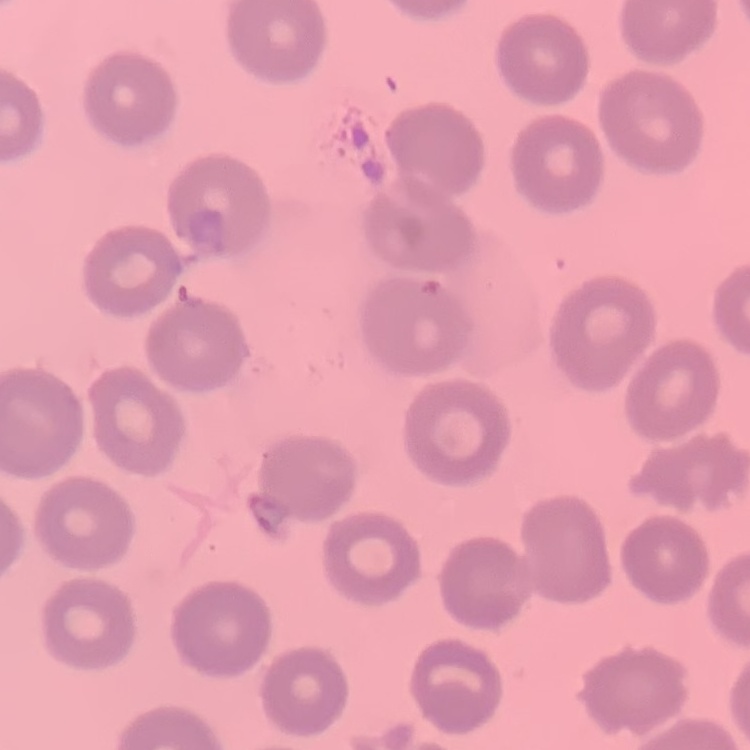
erythrocyte_morphology: no rouleaux formation
stain: Field's or Giemsa
preparation: thin blood smear
image_type: one tile cut from a larger photomicrograph